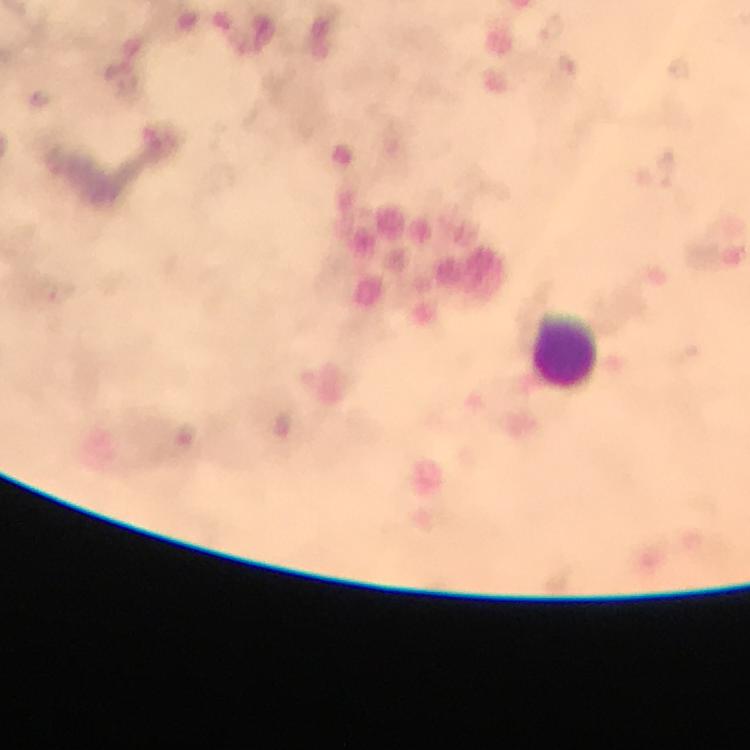

Approximate centers as (x, y) in pixels.
Summary:
  - Leukocyte locations: (566, 350)
  - Context: from a diagnostic examination for malaria
  - Image size: 750×750 pixels
  - Capture: smartphone camera through the microscope
  - Plasmodium parasites: none seen
  - Preparation: thick blood smear
  - Cropped from: one field of view
  - Stain: Giemsa
  - Magnification: 100x
  - Immersion oil: applied